Assess this cell for malaria.
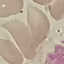
It is uninfected.

Summary:
  - Image type: automatically extracted cell patch, resized to 64 × 64 pixels
  - Stain: Giemsa
  - Capture: smartphone camera at the microscope eyepiece
  - Preparation: thin blood smear